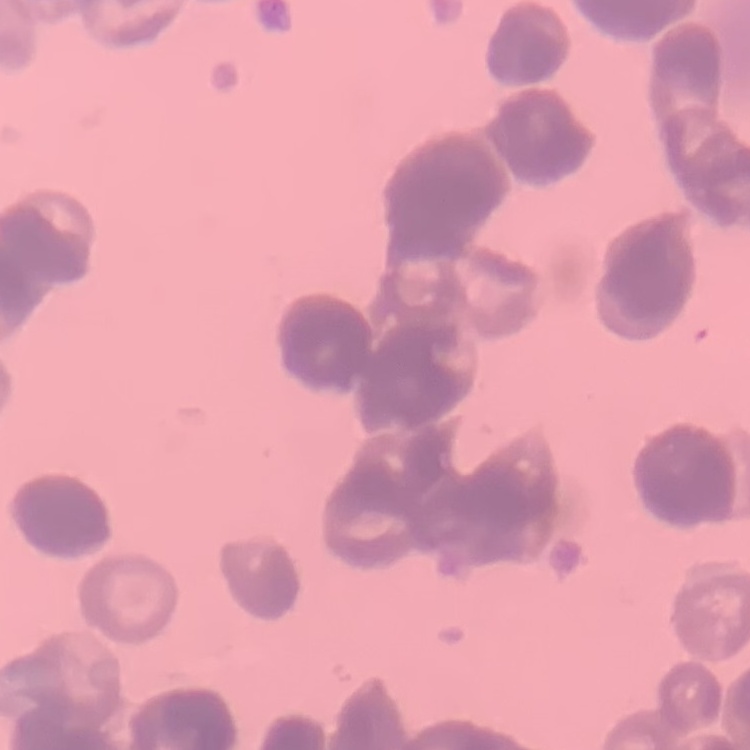

{
  "red_blood_cell_morphology": "rouleaux formation",
  "image_type": "one tile cut from a larger photomicrograph",
  "stain": "Field's or Giemsa",
  "preparation": "thin blood smear"
}